Report the malaria status of this cell.
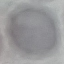

It is uninfected.

capture: smartphone through the microscope eyepiece
stain: Giemsa
image_type: cell patch, automatically extracted from a larger field of view and resized to 64 × 64 pixels
preparation: thin smear